Report the malaria status of this cell.
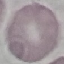
Uninfected.

Summary:
  - Preparation: thin smear
  - Image type: cell patch, automatically extracted from a larger field of view and resized to 64 × 64 pixels
  - Capture: smartphone camera at the microscope eyepiece
  - Stain: Giemsa